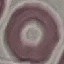 Result: negative for malaria parasites. Photographed with a smartphone camera at the microscope eyepiece. Automatically extracted cell patch, resized to 64 × 64 pixels. Thin blood film. Giemsa-stained preparation.